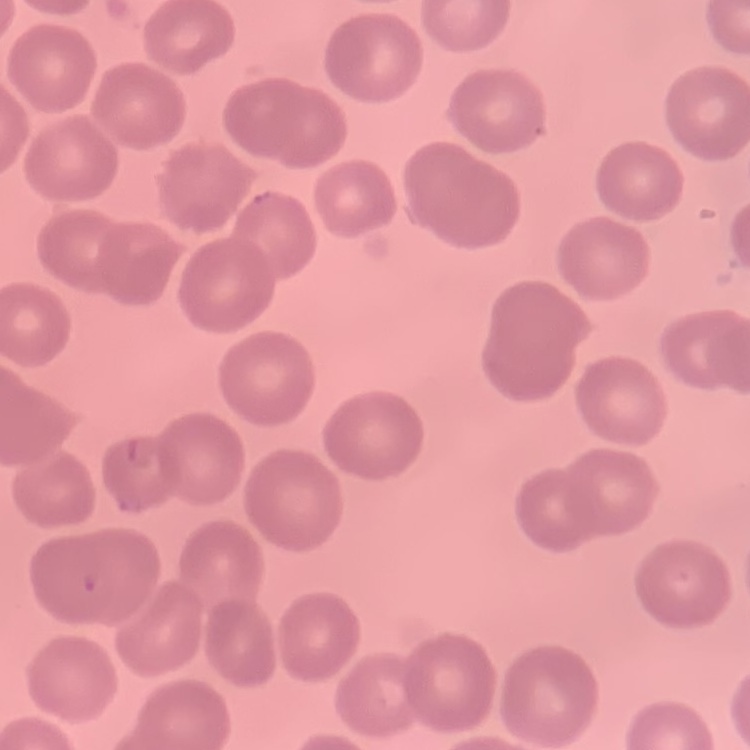

The red blood cells exhibit no rouleaux formation. Field's or Giemsa stain. Thin blood smear. One tile cut from a larger photomicrograph.